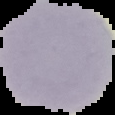
{
  "image_type": "cell region segmented out of the field of view; surrounding area masked to black",
  "result": "no malaria parasites seen",
  "preparation": "thin blood smear",
  "image_size": "115×115 pixels"
}